Outline each uninfected red blood cell.
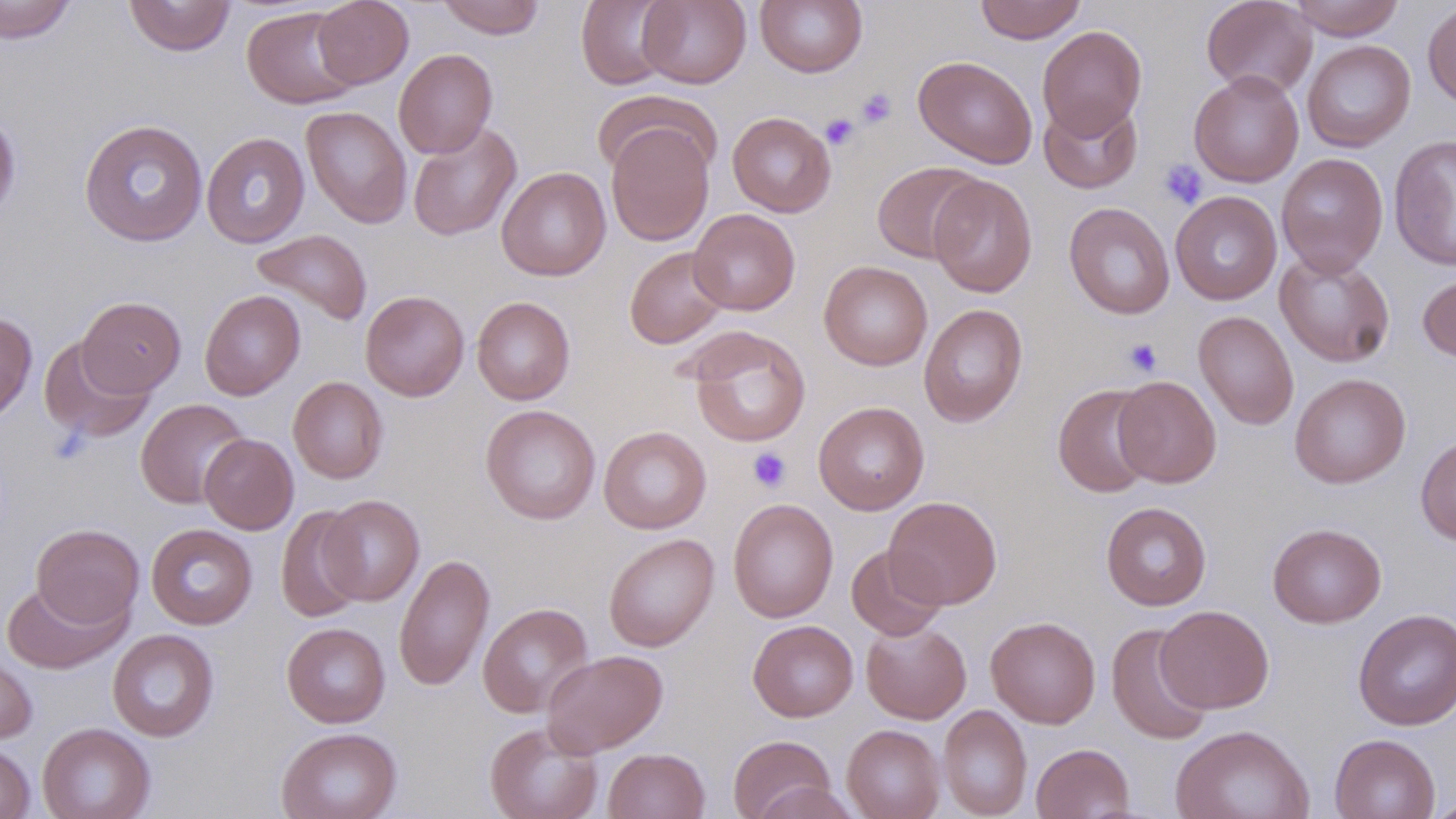
Approximate bounding boxes as (x1, y1, x2, y2) in pixels.
Uninfected red blood cells: (0, 0, 77, 44), (123, 0, 236, 56), (313, 0, 414, 89), (436, 0, 546, 39), (576, 0, 677, 89), (638, 0, 751, 89), (754, 0, 868, 77), (975, 0, 1086, 43), (1201, 0, 1318, 99), (1288, 0, 1405, 40), (1422, 2, 1456, 109), (242, 6, 360, 109), (1037, 25, 1148, 139), (1302, 39, 1416, 152), (394, 48, 497, 158), (913, 55, 1038, 169), (1189, 70, 1304, 187), (591, 91, 719, 181), (1038, 97, 1143, 194), (301, 105, 412, 228), (0, 111, 21, 221), (727, 112, 836, 217), (79, 118, 208, 246), (605, 120, 715, 247), (408, 122, 522, 241), (201, 132, 311, 249), (1388, 135, 1456, 271), (1276, 153, 1389, 277), (871, 161, 986, 264), (497, 167, 611, 281), (928, 174, 1038, 297), (1170, 191, 1282, 305), (1063, 202, 1175, 320), (688, 208, 800, 315), (251, 229, 373, 325), (624, 246, 729, 349), (1275, 249, 1396, 367), (819, 261, 932, 370), (1417, 269, 1456, 364), (199, 289, 305, 400), (360, 290, 469, 401), (78, 296, 185, 397), (471, 296, 575, 405), (918, 304, 1028, 427), (1193, 311, 1299, 430), (0, 312, 37, 422), (685, 326, 811, 448), (38, 337, 155, 444), (1289, 373, 1411, 489), (1113, 375, 1221, 487), (288, 376, 388, 484), (1052, 383, 1159, 498), (135, 398, 250, 509), (813, 401, 929, 515), (480, 404, 601, 525), (598, 426, 712, 533), (199, 433, 299, 534), (1415, 433, 1456, 545), (320, 494, 424, 605), (883, 496, 1003, 609), (727, 498, 838, 623), (1101, 502, 1212, 610), (276, 505, 368, 622), (31, 523, 144, 630), (1267, 523, 1386, 628), (146, 524, 257, 630), (603, 533, 719, 652), (846, 544, 947, 641), (394, 552, 495, 692), (2, 581, 128, 674), (478, 602, 593, 718), (1156, 605, 1274, 713), (1353, 608, 1456, 730), (985, 615, 1101, 728), (748, 620, 859, 721), (860, 620, 972, 724), (281, 622, 391, 727), (1107, 623, 1214, 745), (107, 629, 220, 742), (0, 649, 37, 745), (541, 650, 668, 757), (938, 704, 1032, 819), (37, 722, 155, 819), (485, 722, 603, 819), (842, 724, 945, 819), (1170, 724, 1315, 819), (276, 727, 401, 819), (1329, 733, 1441, 819), (728, 734, 838, 819), (0, 741, 36, 818), (1031, 742, 1135, 819), (603, 748, 710, 819), (751, 781, 861, 819), (1428, 795, 1456, 819).

slide-level diagnosis = negative for blood parasites
platelet locations = approximate bounding boxes as (x1, y1, x2, y2) in pixels: (856, 88, 896, 128), (819, 113, 860, 150), (1158, 159, 1208, 210), (1123, 338, 1163, 376), (748, 447, 791, 492)
image size = 1456×819 pixels
modality = optical microscopy
preparation = thin blood smear
stain = May-Grünwald-Giemsa
magnification = 1000x
field of view = one of a larger specimen